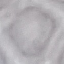
Summary:
  - Malaria status: uninfected
  - Preparation: thin blood smear
  - Image type: cell patch, automatically extracted from a larger field of view and resized to 64 × 64 pixels
  - Capture: smartphone through the microscope eyepiece
  - Stain: Giemsa